Classify this cell by malaria status.
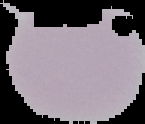

It is uninfected.

image size = 145×124 pixels
preparation = thin blood smear
image type = segmented cell region on a black background